Outline each blood parasite and name the species.
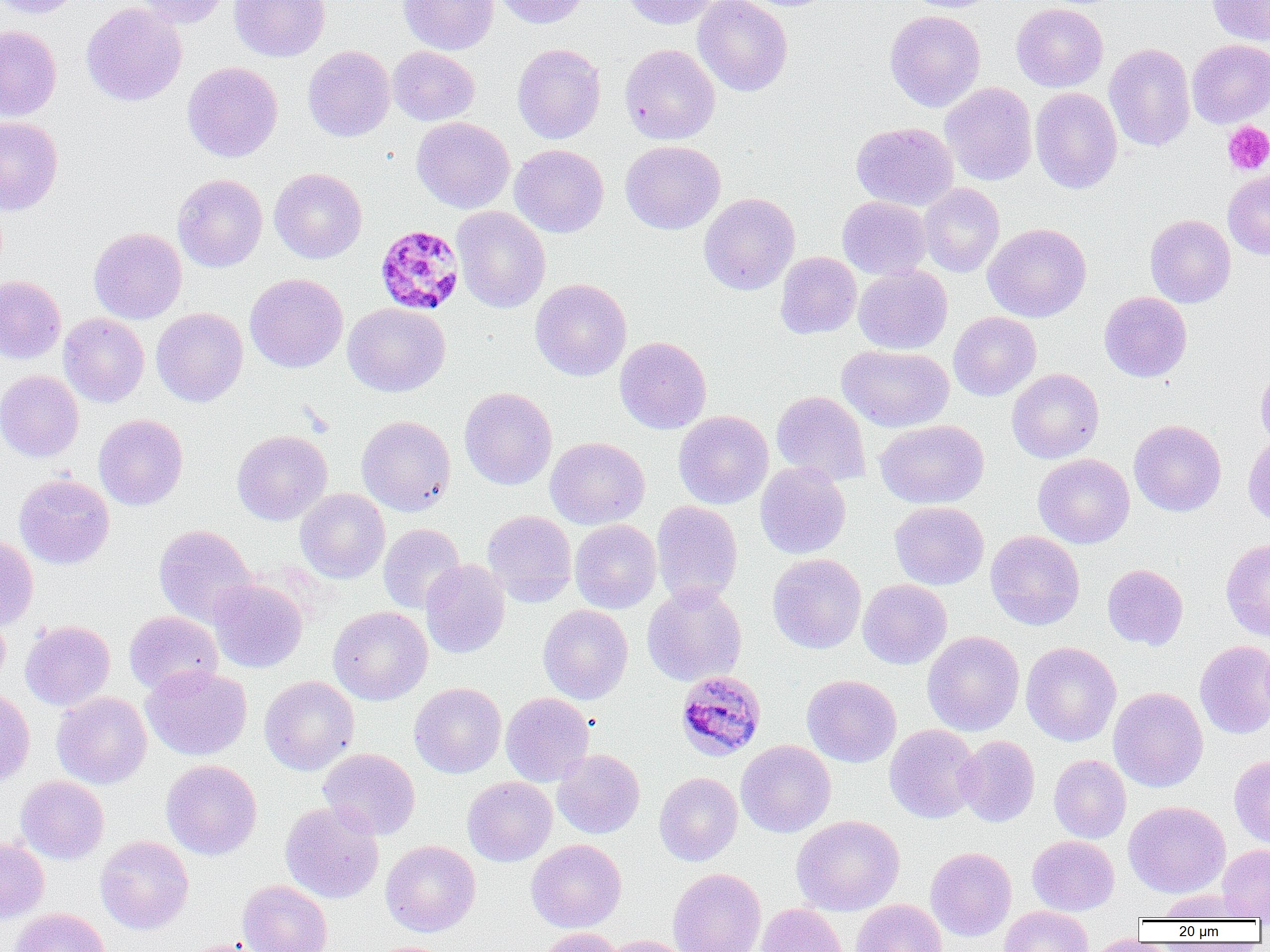
Approximate bounding boxes as named x1/y1/x2/y2 corners in pixels.
Plasmodium malariae-infected red blood cells: (x1=375, y1=224, x2=465, y2=316), (x1=674, y1=670, x2=766, y2=761).
No Plasmodium falciparum, Plasmodium ovale, Plasmodium vivax, Babesia divergens, or Trypanosoma brucei observed.

Uninfected red blood cell locations: (x1=0, y1=0, x2=85, y2=19), (x1=132, y1=0, x2=229, y2=29), (x1=229, y1=0, x2=330, y2=62), (x1=398, y1=0, x2=499, y2=55), (x1=494, y1=0, x2=593, y2=28), (x1=623, y1=0, x2=720, y2=29), (x1=693, y1=0, x2=792, y2=96), (x1=903, y1=0, x2=999, y2=13), (x1=1207, y1=0, x2=1270, y2=45), (x1=1011, y1=2, x2=1108, y2=92), (x1=81, y1=3, x2=187, y2=107), (x1=885, y1=10, x2=986, y2=112), (x1=0, y1=25, x2=61, y2=121), (x1=1187, y1=39, x2=1270, y2=128), (x1=1104, y1=42, x2=1196, y2=151), (x1=512, y1=43, x2=606, y2=144), (x1=619, y1=43, x2=720, y2=145), (x1=303, y1=45, x2=395, y2=141), (x1=388, y1=46, x2=479, y2=126), (x1=182, y1=61, x2=283, y2=162), (x1=940, y1=82, x2=1037, y2=186), (x1=1030, y1=87, x2=1123, y2=194), (x1=0, y1=117, x2=63, y2=215), (x1=411, y1=117, x2=515, y2=213), (x1=851, y1=122, x2=958, y2=211), (x1=620, y1=140, x2=725, y2=234), (x1=510, y1=144, x2=608, y2=237), (x1=269, y1=168, x2=367, y2=264), (x1=1223, y1=170, x2=1270, y2=260), (x1=173, y1=174, x2=268, y2=272), (x1=918, y1=183, x2=1005, y2=277), (x1=698, y1=192, x2=799, y2=295), (x1=837, y1=196, x2=930, y2=280), (x1=451, y1=206, x2=550, y2=313), (x1=1145, y1=214, x2=1236, y2=307), (x1=983, y1=223, x2=1091, y2=322), (x1=89, y1=227, x2=187, y2=324), (x1=774, y1=251, x2=861, y2=339), (x1=853, y1=264, x2=952, y2=354), (x1=245, y1=272, x2=348, y2=373), (x1=0, y1=275, x2=66, y2=364), (x1=531, y1=278, x2=632, y2=381), (x1=1099, y1=291, x2=1192, y2=382), (x1=343, y1=302, x2=450, y2=396), (x1=151, y1=308, x2=248, y2=407), (x1=948, y1=311, x2=1041, y2=401), (x1=59, y1=313, x2=149, y2=407), (x1=615, y1=336, x2=712, y2=434), (x1=837, y1=345, x2=954, y2=432), (x1=1256, y1=364, x2=1270, y2=451), (x1=0, y1=369, x2=84, y2=462), (x1=1007, y1=369, x2=1104, y2=463), (x1=459, y1=387, x2=557, y2=489), (x1=771, y1=390, x2=871, y2=485), (x1=673, y1=411, x2=774, y2=509), (x1=93, y1=414, x2=188, y2=511), (x1=357, y1=415, x2=456, y2=515), (x1=874, y1=419, x2=989, y2=509), (x1=1129, y1=420, x2=1226, y2=517), (x1=232, y1=429, x2=332, y2=525), (x1=1243, y1=433, x2=1270, y2=527), (x1=545, y1=437, x2=650, y2=529), (x1=1033, y1=454, x2=1135, y2=548), (x1=755, y1=461, x2=851, y2=559), (x1=14, y1=474, x2=114, y2=569), (x1=295, y1=488, x2=390, y2=583), (x1=652, y1=501, x2=743, y2=607), (x1=889, y1=501, x2=989, y2=590), (x1=482, y1=510, x2=577, y2=605), (x1=570, y1=519, x2=662, y2=613), (x1=378, y1=523, x2=465, y2=613), (x1=154, y1=524, x2=256, y2=627), (x1=985, y1=530, x2=1085, y2=630), (x1=0, y1=536, x2=38, y2=630), (x1=1221, y1=538, x2=1270, y2=641), (x1=767, y1=553, x2=866, y2=654), (x1=421, y1=559, x2=510, y2=659), (x1=1102, y1=564, x2=1188, y2=650), (x1=208, y1=578, x2=308, y2=673), (x1=858, y1=579, x2=952, y2=669), (x1=642, y1=584, x2=747, y2=686), (x1=538, y1=604, x2=633, y2=704), (x1=328, y1=606, x2=432, y2=705), (x1=0, y1=607, x2=10, y2=688), (x1=124, y1=611, x2=223, y2=695), (x1=20, y1=620, x2=115, y2=711), (x1=922, y1=631, x2=1024, y2=735), (x1=1194, y1=639, x2=1270, y2=739), (x1=1021, y1=641, x2=1121, y2=746), (x1=141, y1=665, x2=252, y2=760), (x1=802, y1=674, x2=902, y2=767), (x1=259, y1=675, x2=359, y2=775), (x1=409, y1=682, x2=506, y2=778), (x1=0, y1=687, x2=35, y2=786), (x1=1108, y1=687, x2=1208, y2=792), (x1=52, y1=692, x2=151, y2=789), (x1=501, y1=692, x2=594, y2=786), (x1=884, y1=724, x2=982, y2=824), (x1=955, y1=735, x2=1039, y2=827), (x1=736, y1=740, x2=836, y2=838), (x1=318, y1=748, x2=420, y2=840), (x1=552, y1=749, x2=645, y2=838), (x1=1049, y1=754, x2=1131, y2=843), (x1=1229, y1=754, x2=1270, y2=849), (x1=161, y1=760, x2=262, y2=859), (x1=654, y1=772, x2=742, y2=866), (x1=16, y1=775, x2=109, y2=864), (x1=462, y1=776, x2=557, y2=867), (x1=280, y1=801, x2=384, y2=903), (x1=1123, y1=801, x2=1230, y2=897), (x1=791, y1=815, x2=905, y2=915), (x1=95, y1=835, x2=193, y2=934), (x1=1027, y1=835, x2=1119, y2=915), (x1=0, y1=837, x2=49, y2=923), (x1=526, y1=839, x2=626, y2=932), (x1=381, y1=840, x2=480, y2=937), (x1=1218, y1=844, x2=1270, y2=921), (x1=925, y1=847, x2=1017, y2=941), (x1=668, y1=867, x2=766, y2=952), (x1=237, y1=879, x2=332, y2=952), (x1=1158, y1=888, x2=1251, y2=920), (x1=852, y1=899, x2=947, y2=952), (x1=756, y1=903, x2=848, y2=952), (x1=999, y1=905, x2=1094, y2=952), (x1=9, y1=908, x2=110, y2=952), (x1=536, y1=927, x2=626, y2=952), (x1=602, y1=935, x2=694, y2=952), (x1=1086, y1=935, x2=1170, y2=952), (x1=172, y1=939, x2=265, y2=952). Platelet locations: (x1=1222, y1=121, x2=1270, y2=175). Slide-level diagnosis: Plasmodium malariae. 1000x magnification. Image is 1270×952 pixels. Single field of view. Thin blood film. Optical microscopy.